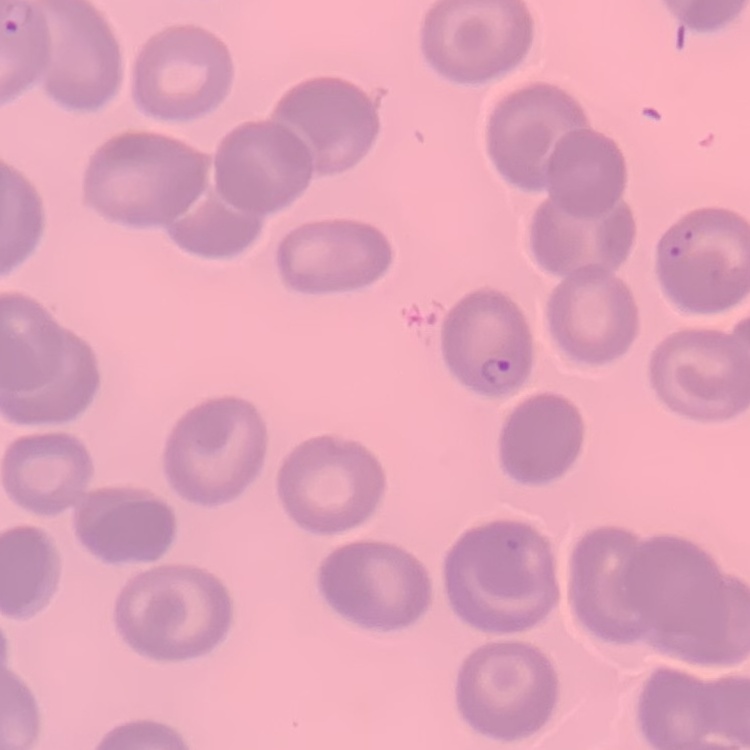
The erythrocytes exhibit no rouleaux formation. Square crop of a larger photomicrograph. Field's or Giemsa stain. Thin peripheral smear.